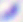
Summary:
  - Identification: Toxoplasma gondii
  - Magnification: 400x
  - Modality: photomicrograph